Assess this cell for malaria.
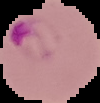
It is parasitized.

image type = cell region segmented out of the field of view; surrounding area masked to black
preparation = thin blood smear
image size = 100×103 pixels